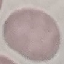

malaria status = uninfected
image type = cell patch, automatically extracted from a larger field of view and resized to 64 × 64 pixels
preparation = thin smear
stain = Giemsa
capture = smartphone camera at the microscope eyepiece